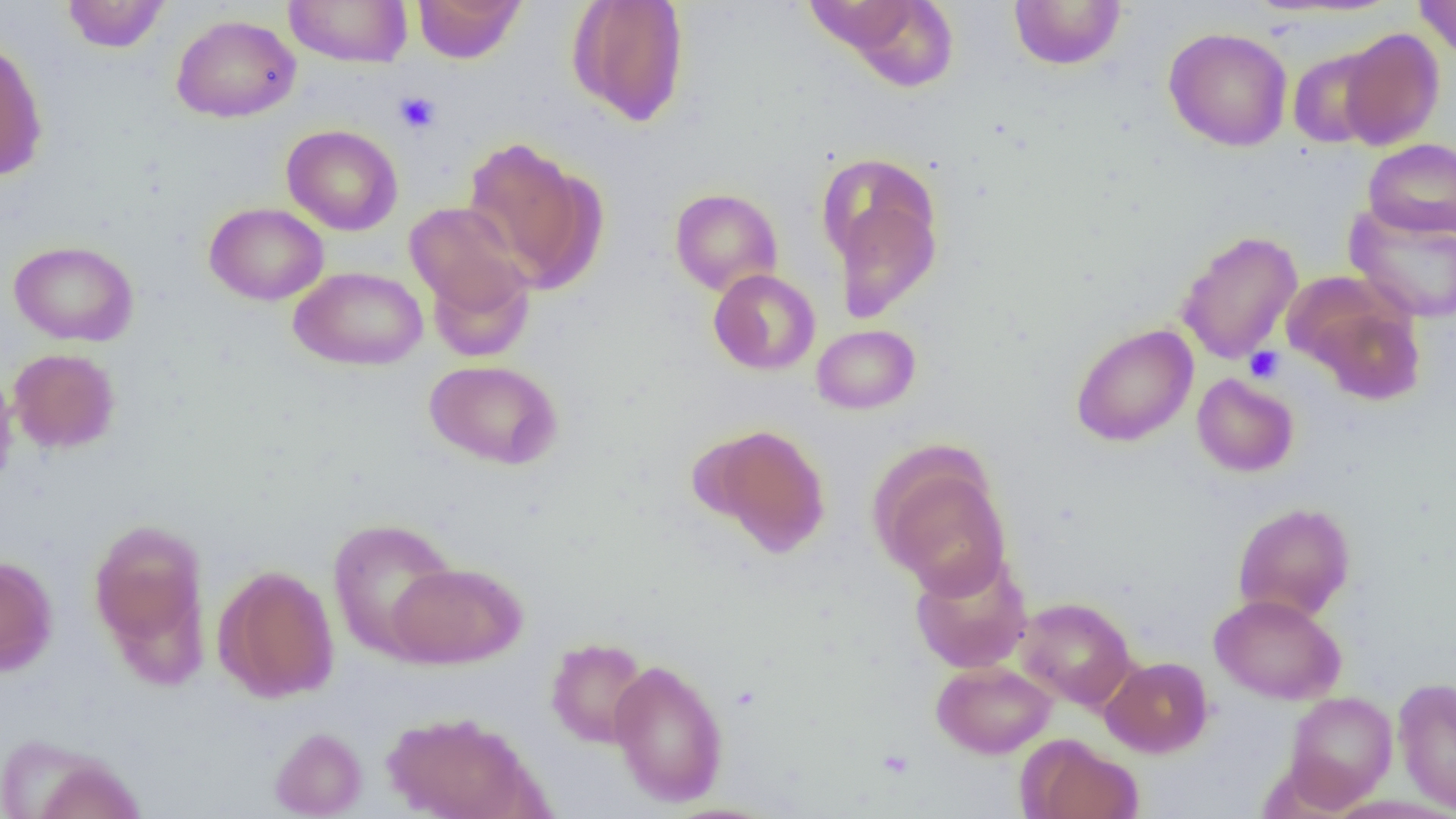
Summary:
  - Coordinate format: approximate bounding boxes as (x1,y1)-(x2,y2) corner pairs in pixels
  - Platelet locations: (394,91)-(442,133), (1244,345)-(1285,384)
  - Uninfected red blood cell locations: (61,0)-(171,53), (284,0)-(412,67), (412,0)-(526,64), (567,0)-(690,126), (818,0)-(961,90), (1414,0)-(1456,61), (1009,1)-(1126,70), (171,14)-(300,123), (1163,27)-(1293,151), (1338,27)-(1445,150), (0,39)-(48,181), (1287,47)-(1388,148), (281,124)-(403,235), (461,136)-(603,291), (1362,138)-(1456,239), (669,187)-(783,296), (830,187)-(941,323), (404,201)-(533,328), (204,202)-(329,305), (1345,203)-(1456,324), (1176,230)-(1302,365), (9,240)-(139,347), (424,253)-(536,365), (289,266)-(428,371), (708,269)-(821,375), (1294,282)-(1427,404), (1070,323)-(1198,447), (811,324)-(920,414), (8,348)-(121,454), (424,359)-(563,469), (0,366)-(18,494), (1192,373)-(1299,477), (703,423)-(830,555), (873,451)-(1011,596), (1232,502)-(1356,622), (327,517)-(460,660), (89,518)-(209,666), (909,551)-(1033,673), (0,555)-(58,676), (388,561)-(526,669), (214,563)-(340,702), (1209,593)-(1346,704), (1016,597)-(1136,710), (546,637)-(651,749), (1100,656)-(1213,757), (609,658)-(728,806), (931,660)-(1057,758), (1393,677)-(1456,813), (1284,691)-(1397,807), (381,710)-(541,819), (269,727)-(367,818), (1018,734)-(1143,819), (21,748)-(146,819)
  - Slide-level diagnosis: negative for blood parasites
  - Magnification: 1000x
  - Preparation: thin blood smear
  - Field of view: single
  - Modality: light microscopy
  - Image size: 1456×819 pixels